Classify this cell by malaria status.
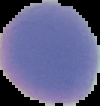

Uninfected.

From a thin blood smear. The area outside the segmented cell region is set to black. Image is 100×106 pixels.